State which parasite is depicted.
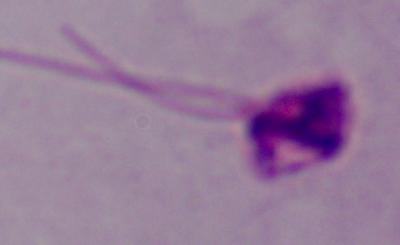
This is Leishmania.

magnification = 1000x
modality = micrograph